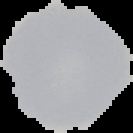

image_type: segmented cell region on a black background
result: no Plasmodium parasites detected
preparation: thin blood film
image_size: 133×133 pixels